Describe the morphology of the red blood cells.
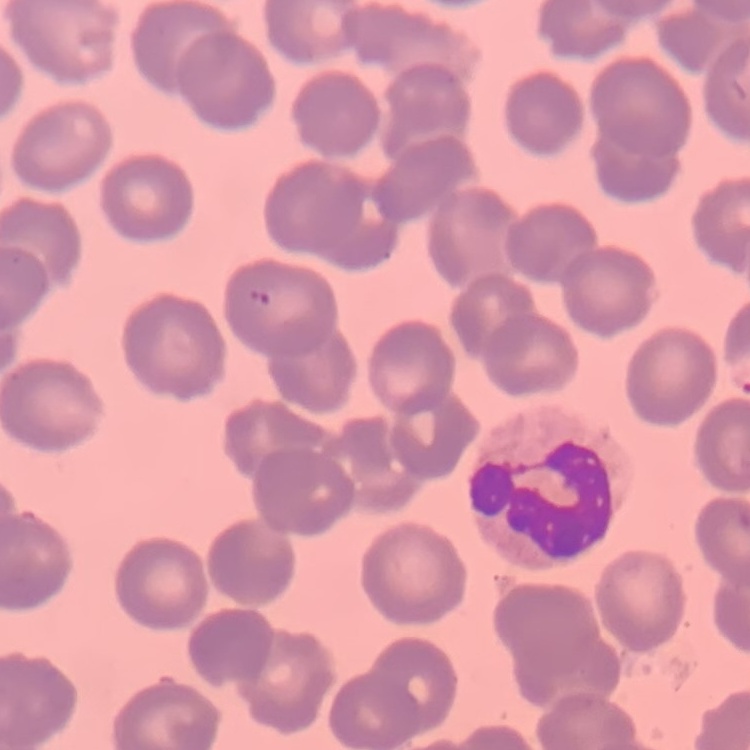
They show no rouleaux formation.

{
  "preparation": "thin peripheral smear",
  "image_type": "one tile cut from a larger photomicrograph",
  "stain": "Field's or Giemsa"
}